Comment on the morphology of the erythrocytes.
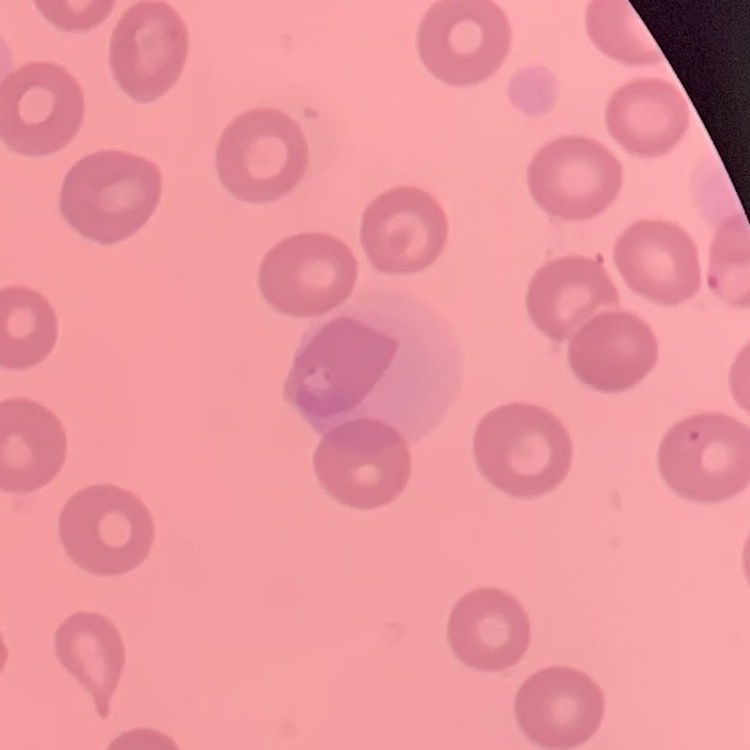

They show no rouleaux formation.

preparation: thin peripheral smear
image_type: one tile cut from a larger photomicrograph
stain: Field's or Giemsa